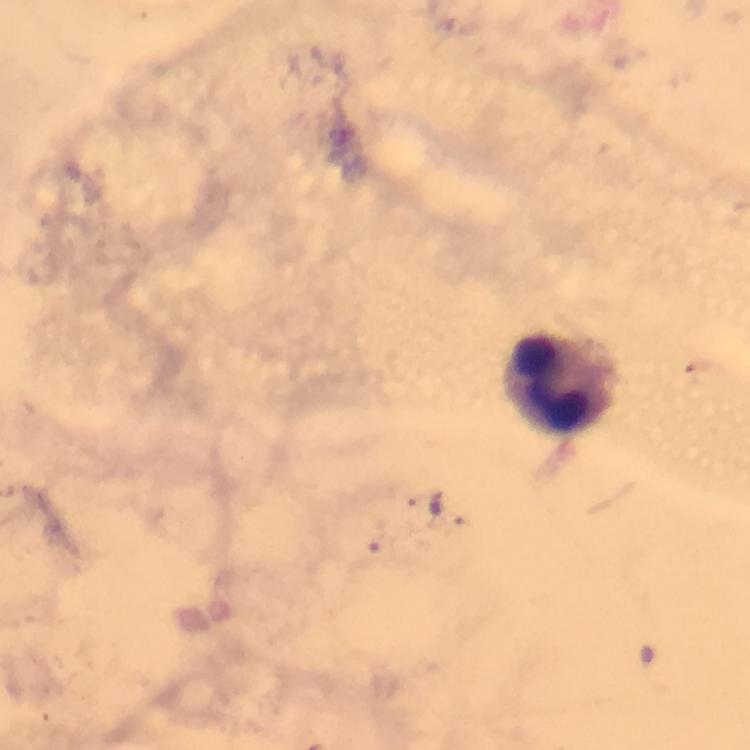 Approximate centers as (x, y) in pixels. Leukocyte locations: (561, 379). 100x magnification. Thick blood smear. Giemsa-stained preparation. Malaria parasites: none detected. Immersion oil was used. Image is 750×750 pixels. Photographed with a smartphone mounted on the microscope. From a malaria diagnostic workup. Cropped region of a single field of view.